Locate every Plasmodium parasite.
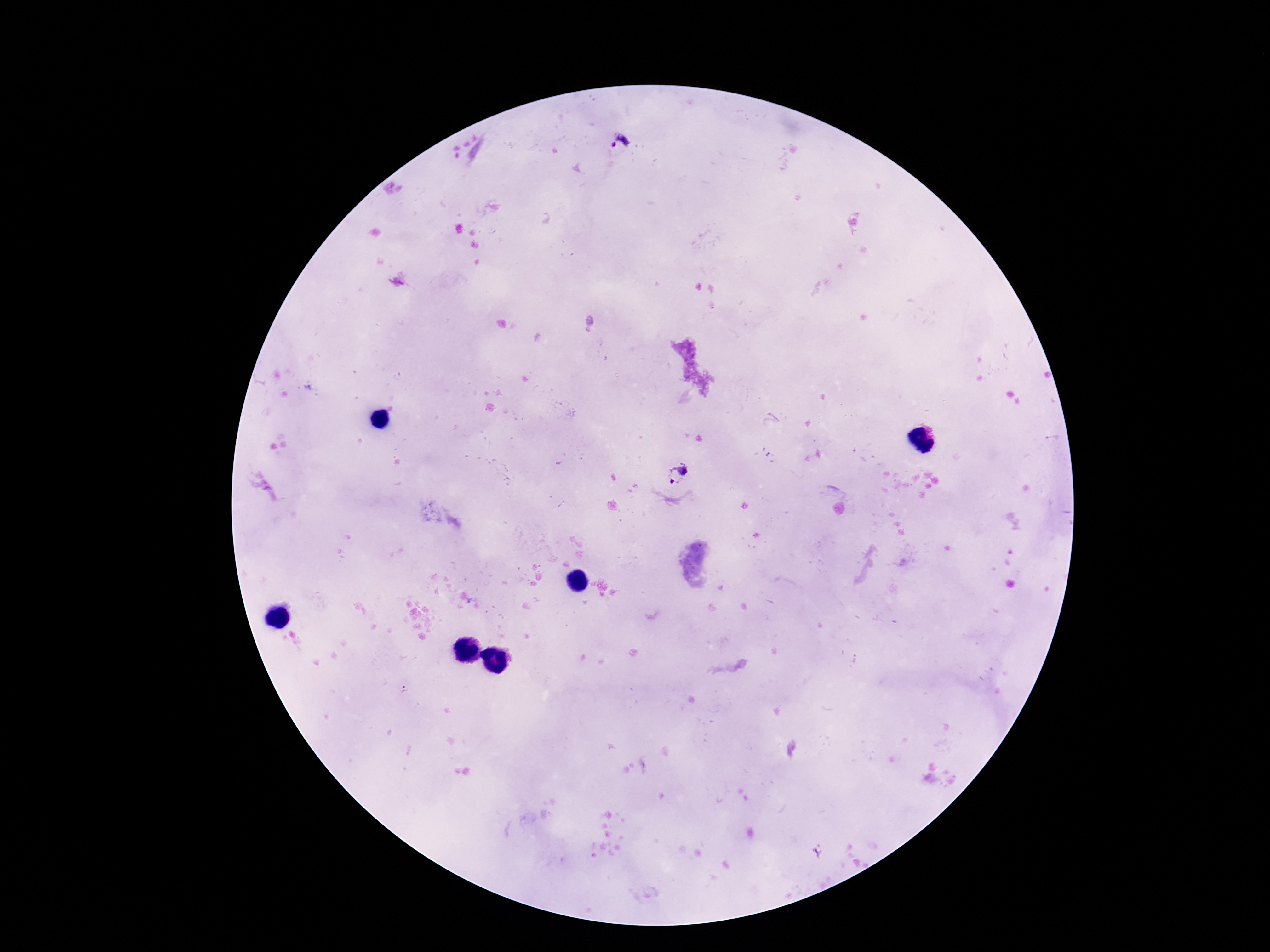
Approximate centers as [x, y] in pixels.
Plasmodium parasites: [621, 145], [680, 474].

patient_malaria_status: infected
magnification: 100x
preparation: thick blood film
field_of_view: one from this slide
stain: Giemsa
image_size: 1270×952 pixels
capture: smartphone camera through the microscope eyepiece